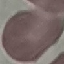
Summary:
  - Malaria status: uninfected
  - Preparation: thin smear
  - Stain: Giemsa
  - Image type: cell patch, automatically extracted from a larger field of view and resized to 64 × 64 pixels
  - Capture: smartphone camera at the microscope eyepiece